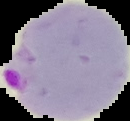

Summary:
  - Preparation: thin blood film
  - Image size: 130×121 pixels
  - Malaria status: parasitized
  - Image type: segmented cell region on a black background